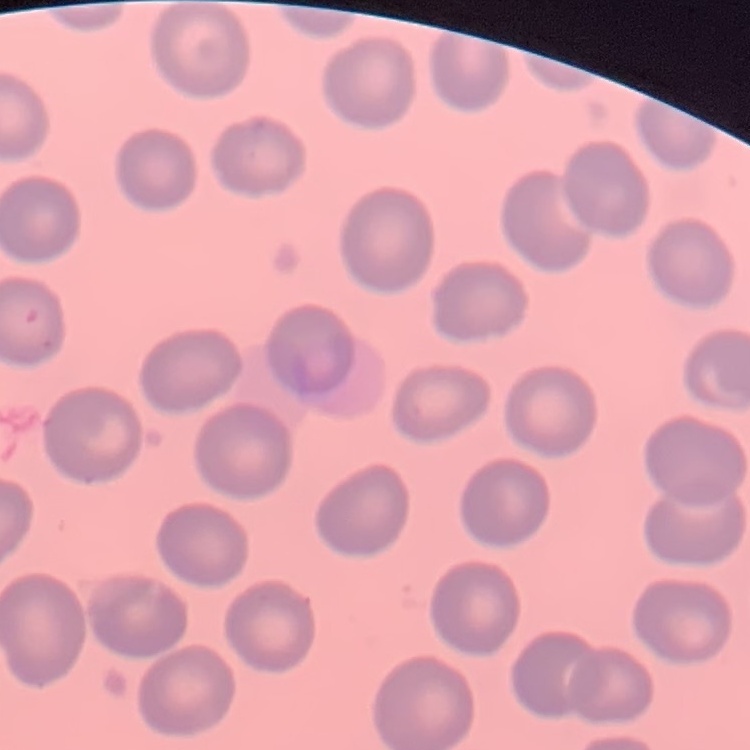
Summary:
  - Erythrocyte morphology: no rouleaux formation
  - Stain: Field's or Giemsa
  - Image type: one tile cut from a larger photomicrograph
  - Preparation: thin blood film